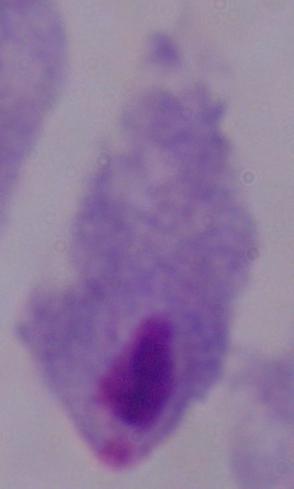 A trichomonad is shown. 1000x magnification. Photomicrograph.